Report the malaria status of this cell.
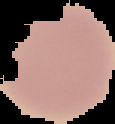

Uninfected.

Image is 115×124 pixels. From a thin blood smear. Cell region segmented out of the field of view; the surrounding area is masked to black.